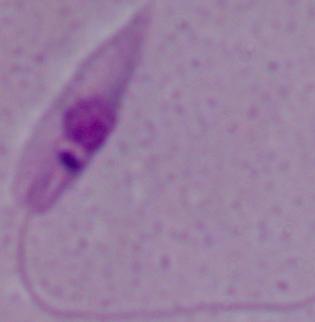
modality: micrograph
magnification: 1000x
identification: Leishmania